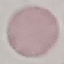

Result: negative for malaria parasites. Thin blood film. Photographed with a smartphone camera at the microscope eyepiece. Giemsa-stained preparation. Automatically extracted cell patch, resized to 64 × 64 pixels.